Point out each Plasmodium parasite.
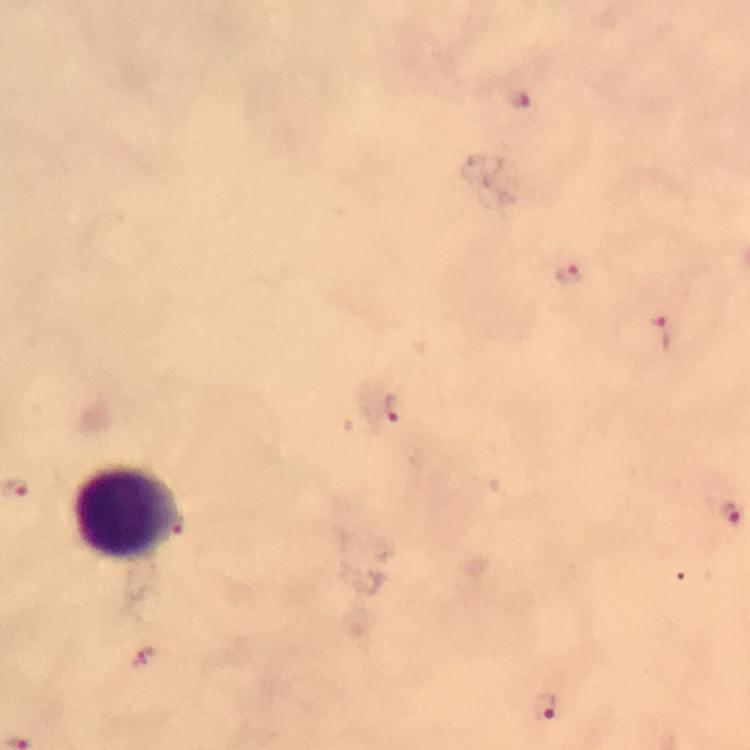
Approximate centers as [x, y] in pixels.
Plasmodium parasites: [517, 97], [567, 273], [658, 332], [390, 407], [730, 513], [178, 522], [142, 658], [544, 709].

Leukocyte locations: [127, 511]. 100x magnification. Image is 750×750 pixels. Thick blood film. Giemsa stain. Immersion oil was used. Cropped region of a single field of view. Photographed through the microscope with a smartphone camera. From a malaria diagnostic workup.